Identify the cell.
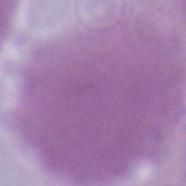
An erythrocyte.

magnification: 1000x
modality: micrograph